Describe the morphology of the erythrocytes.
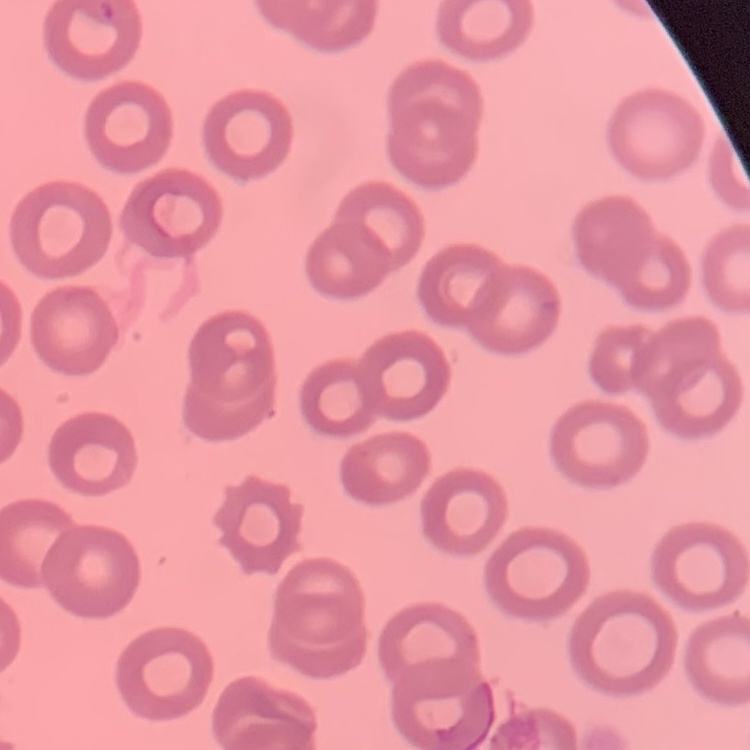
No rouleaux formation.

Summary:
  - Stain: Field's or Giemsa
  - Image type: square crop of a larger photomicrograph
  - Preparation: thin blood film